Identify the cell.
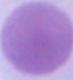

An erythrocyte.

Summary:
  - Modality: micrograph
  - Magnification: 1000x